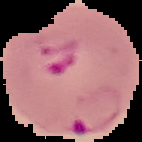
Summary:
  - Malaria status: parasitized
  - Image type: segmented cell region with the area outside set to black
  - Preparation: thin blood film
  - Image size: 142×142 pixels